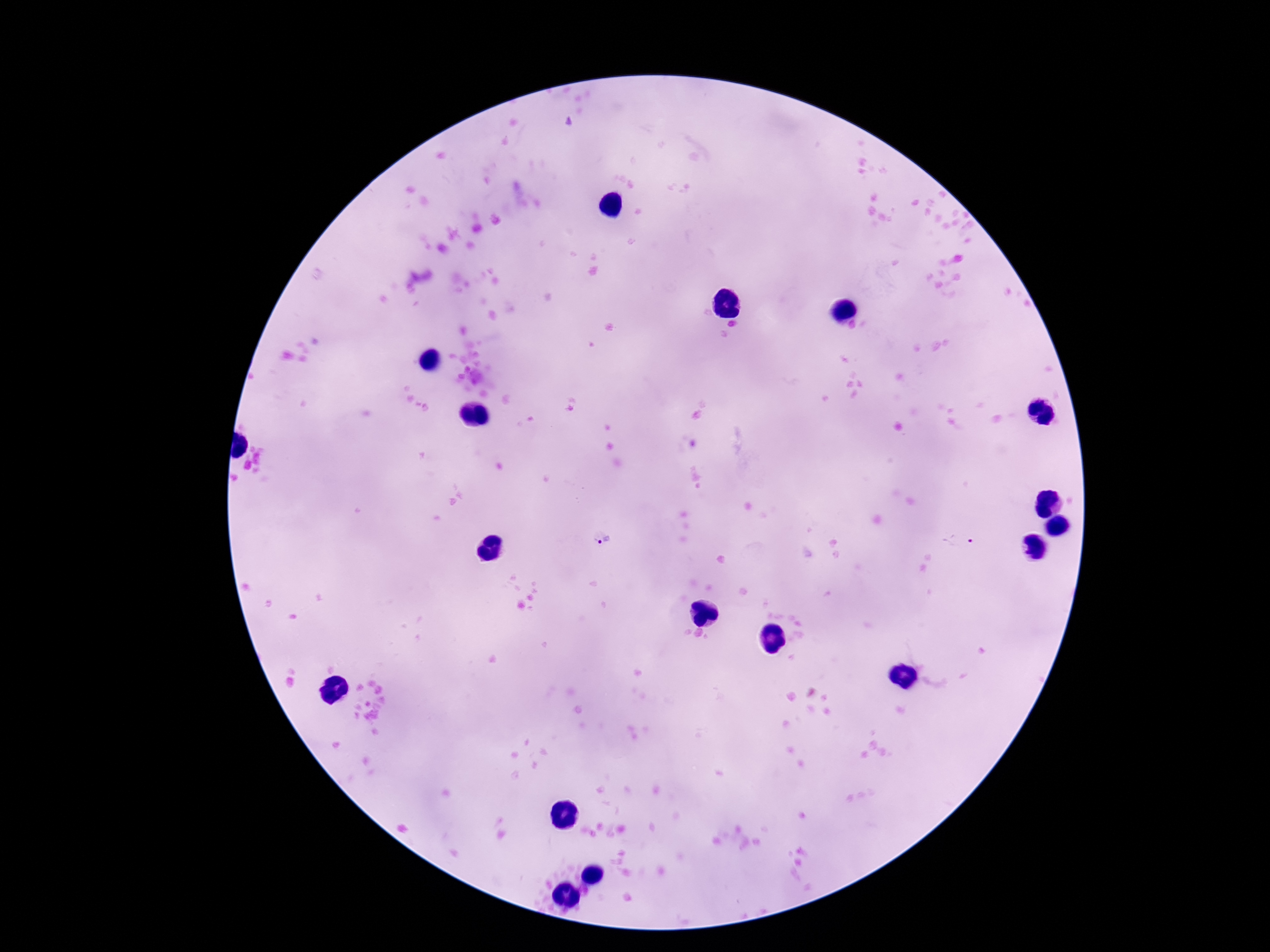

Approximate centers as [x, y] in pixels.
Summary:
  - Plasmodium parasite locations: [570, 126], [603, 539], [960, 540]
  - Patient malaria status: positive
  - Capture: smartphone camera through the microscope eyepiece
  - Image size: 1270×952 pixels
  - Magnification: 100x
  - Preparation: thick blood smear
  - Field of view: one from this slide
  - Stain: Giemsa